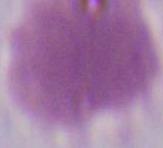
1000x magnification. A red blood cell is shown. Photomicrograph.